Describe the morphology of the red blood cells.
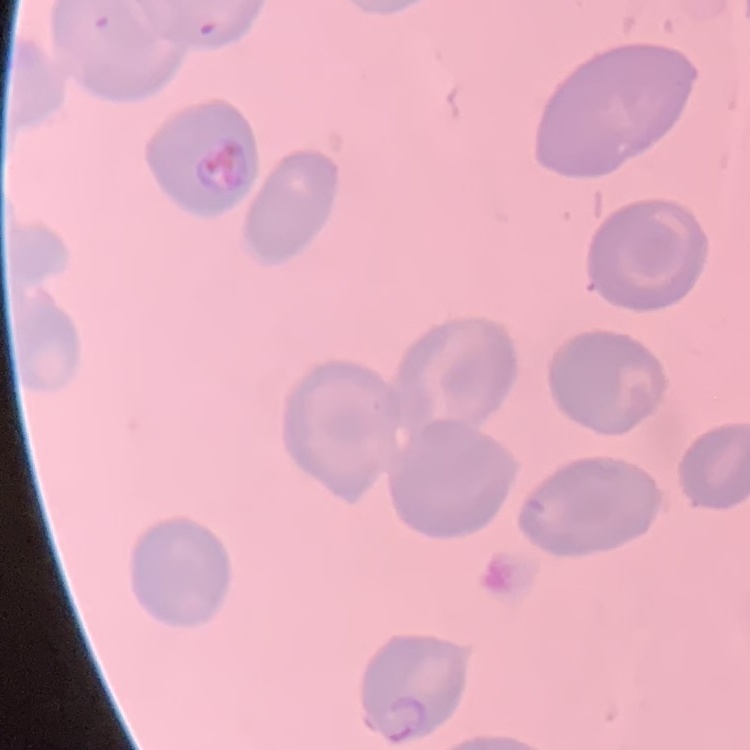
No rouleaux formation.

stain = Field's or Giemsa
preparation = thin blood smear
image type = square crop of a larger photomicrograph